Assess this cell for malaria.
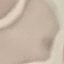
Uninfected.

Giemsa-stained preparation. Acquired by smartphone through the microscope eyepiece. Automatically extracted cell patch, resized to 64 × 64 pixels. Thin blood smear.